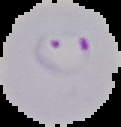 Malaria status: parasitized. Cell region segmented out of the field of view; the surrounding area is masked to black. From a thin blood smear. Image is 121×127 pixels.